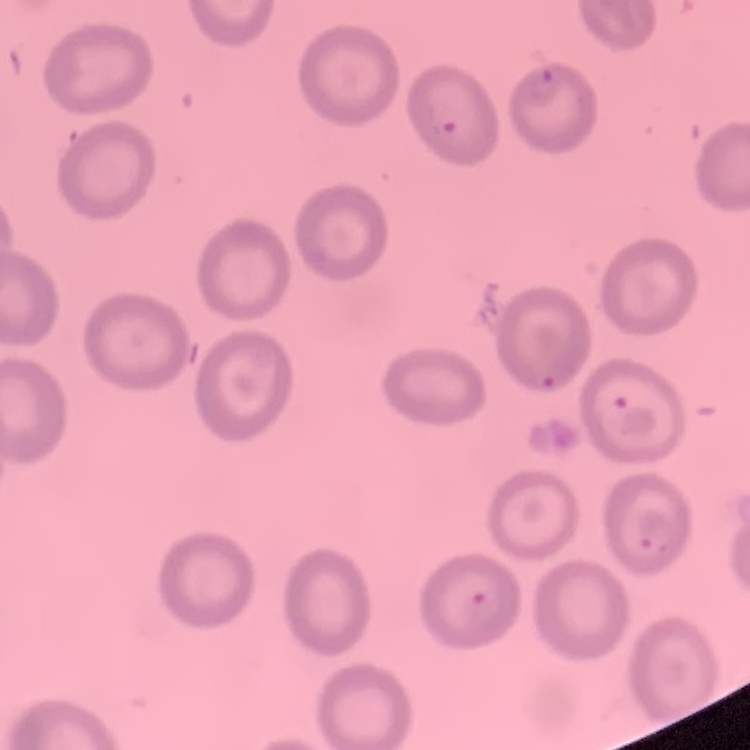
{
  "erythrocyte_morphology": "no rouleaux formation",
  "preparation": "thin blood film",
  "stain": "Field's or Giemsa",
  "image_type": "square crop of a larger photomicrograph"
}